Assess the morphology of the erythrocytes.
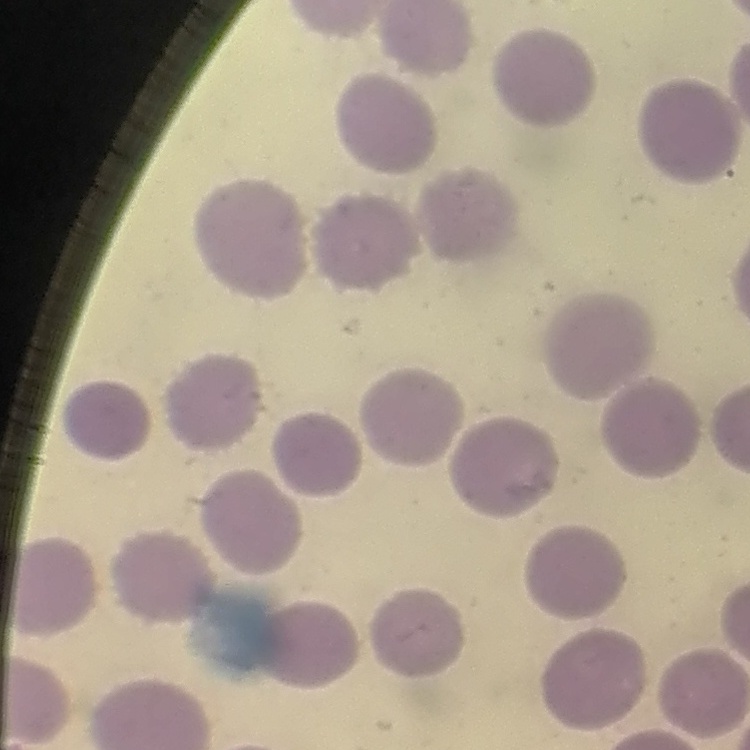
No rouleaux formation.

Thin blood film. Stained with either Field's or Giemsa. Square crop of a larger photomicrograph.